Point out each leukocyte.
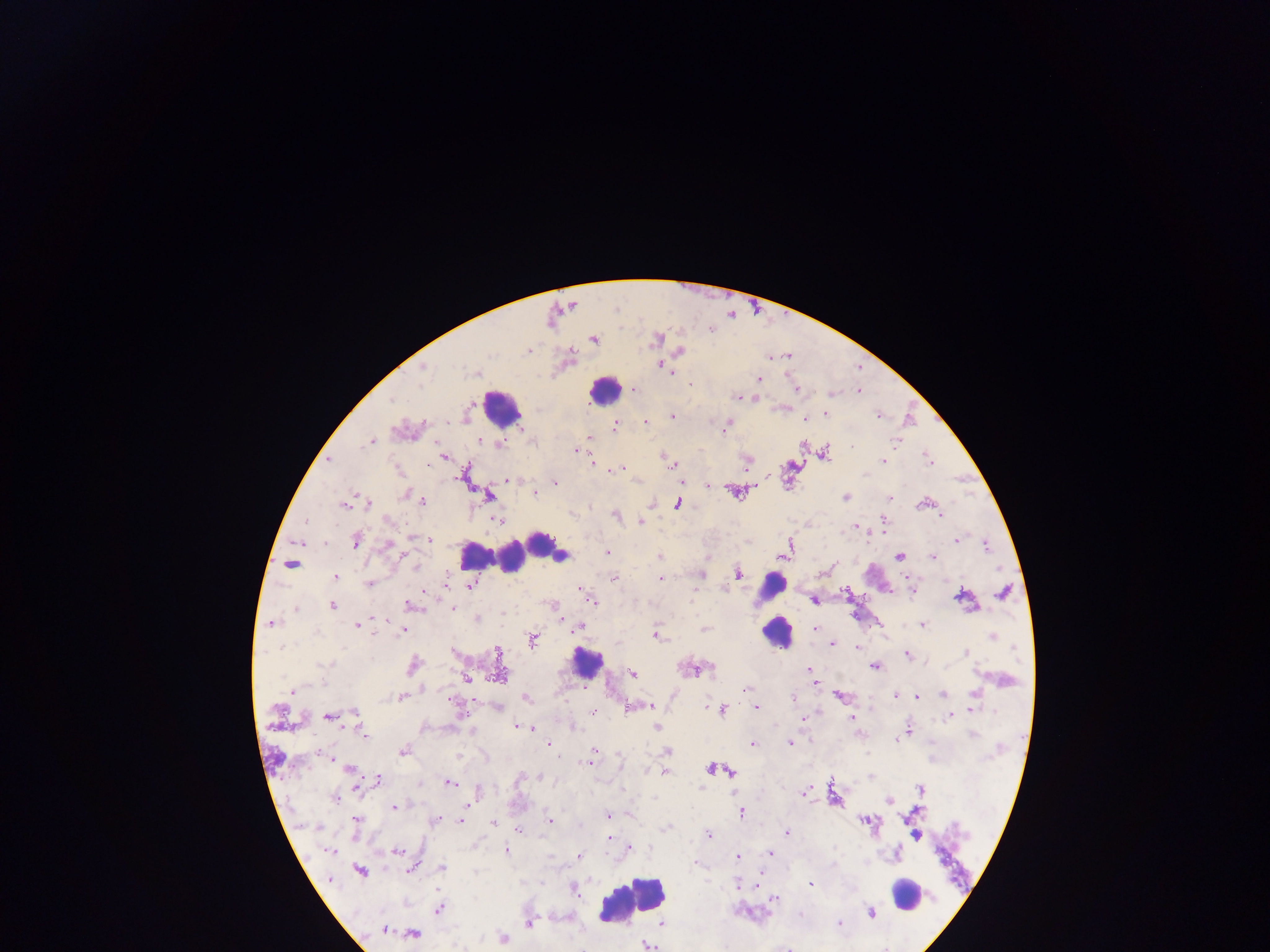
Approximate centers as (x, y) in pixels.
Leukocytes: (604, 391), (502, 408), (545, 545), (478, 557), (512, 557), (772, 586), (776, 632), (586, 662), (910, 895), (633, 901).

Summary:
  - Malaria parasite locations: (594, 339), (655, 340), (528, 350), (681, 351), (423, 366), (662, 366), (668, 370), (758, 379), (691, 385), (634, 390), (796, 390), (858, 391), (831, 394), (737, 397), (825, 414), (673, 416), (878, 416), (805, 419), (646, 422), (726, 426), (614, 427), (522, 428), (589, 437), (479, 441), (369, 442), (499, 444), (852, 447), (577, 450), (824, 455), (927, 456), (445, 457), (330, 460), (883, 461), (428, 465), (672, 465), (619, 469), (508, 480), (555, 483), (708, 485), (534, 493), (736, 493), (406, 495), (488, 497), (845, 497), (888, 498), (422, 501), (678, 503), (366, 504), (922, 504), (345, 505), (941, 515), (616, 516), (387, 520), (498, 520), (884, 520), (641, 522), (855, 526), (884, 530), (414, 538), (356, 540), (430, 540), (956, 540), (324, 543), (388, 543), (789, 544), (986, 545), (608, 552), (660, 556), (899, 556), (933, 557), (292, 563), (738, 572), (702, 574), (335, 577), (615, 578), (660, 578), (369, 584), (471, 586), (581, 590), (1003, 593), (961, 597), (592, 600), (813, 600), (332, 606), (412, 606), (452, 608), (296, 610), (478, 620), (270, 624), (923, 624), (357, 625), (578, 627), (704, 628), (816, 628), (402, 631), (656, 635), (991, 636), (533, 640), (831, 644), (285, 646), (856, 647), (1014, 649), (499, 653), (966, 653), (907, 655), (325, 665), (413, 665), (875, 667), (709, 668), (808, 669), (691, 670), (500, 672), (811, 672), (633, 674), (466, 678), (813, 681), (292, 690), (747, 690), (942, 694), (974, 694), (401, 697), (839, 697), (895, 697), (916, 697), (526, 698), (792, 698), (650, 706), (497, 707), (631, 707), (756, 707), (715, 709), (972, 709), (722, 710), (594, 712), (355, 714), (329, 715), (949, 716), (853, 717), (803, 718), (520, 727), (656, 728), (530, 729), (908, 730), (363, 734), (973, 734), (897, 739), (549, 744), (753, 744), (789, 744), (403, 751), (594, 751), (667, 751), (328, 757), (589, 762), (711, 768), (350, 769), (647, 770), (729, 771), (664, 772), (870, 777), (378, 780), (449, 782), (360, 787), (702, 787), (920, 788), (805, 792), (335, 799), (889, 801), (395, 807), (741, 812), (608, 816), (436, 820), (462, 820), (550, 820), (356, 821), (493, 822), (868, 822), (666, 828), (518, 831), (786, 832), (708, 834), (916, 836), (608, 838), (629, 848), (329, 850), (397, 851), (506, 851), (770, 853), (578, 857), (737, 858), (696, 864), (412, 867), (442, 868), (360, 872), (758, 876), (738, 884), (811, 884), (574, 890), (775, 899), (439, 909), (871, 913), (800, 914), (529, 923), (838, 924), (663, 925), (383, 929), (413, 934), (504, 938), (646, 945)
  - Preparation: thick blood film
  - Image size: 1270×952 pixels
  - Field of view: single
  - Country: Ghana
  - Capture: mobile-phone photograph through a microscope